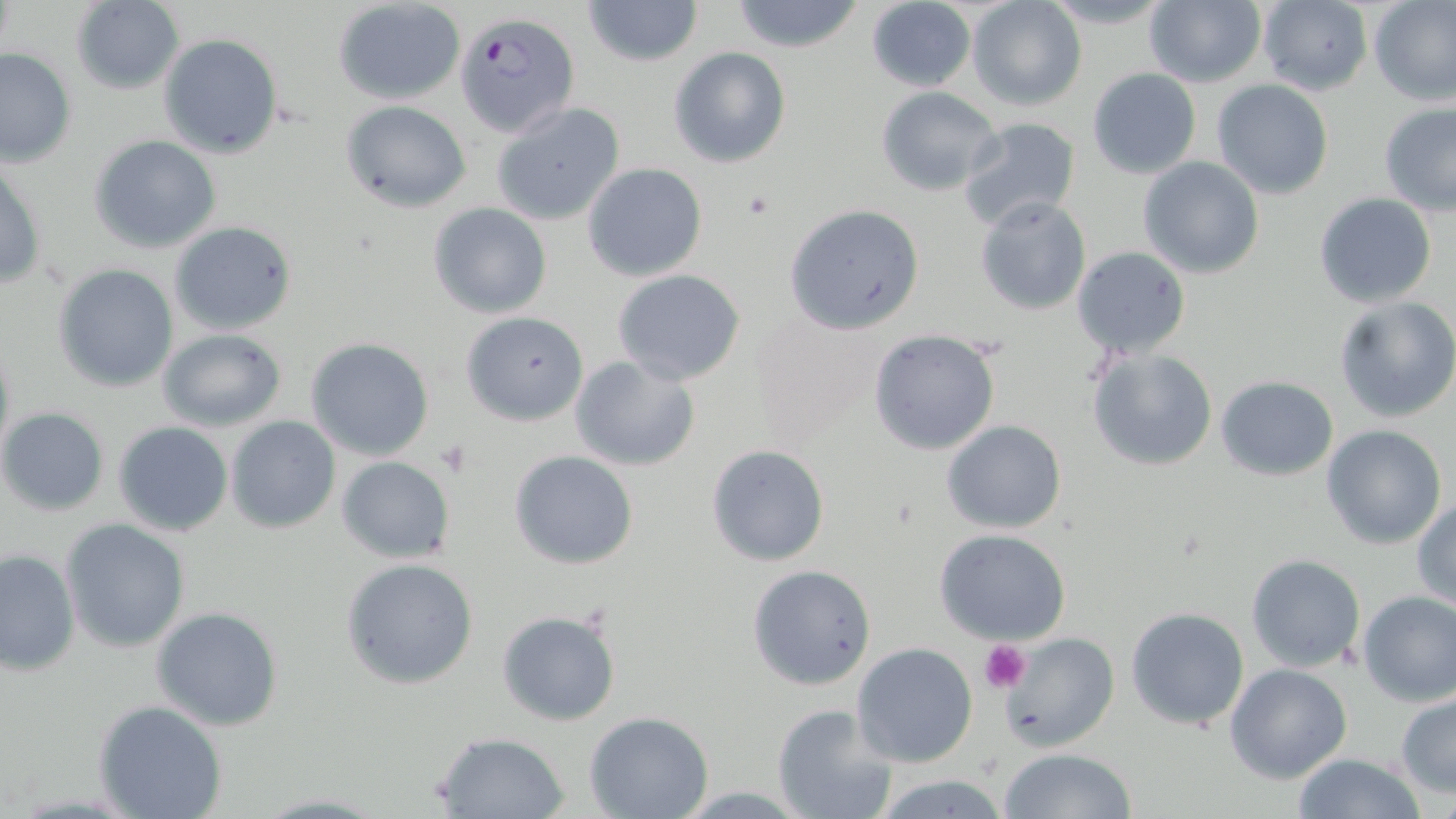
{
  "slide_level_diagnosis": "Plasmodium falciparum",
  "stain": "May-Grünwald-Giemsa",
  "modality": "optical microscopy",
  "magnification": "1000x",
  "uninfected_red_blood_cell_locations": "approximate bounding boxes as (x1,y1)-(x2,y2) corner pairs in pixels: (582,0)-(703,68), (730,0)-(863,52), (866,0)-(976,92), (966,0)-(1086,112), (1040,0)-(1177,31), (1145,0)-(1267,88), (1256,0)-(1374,96), (1369,0)-(1456,107), (69,1)-(184,93), (333,1)-(467,105), (158,33)-(283,159), (668,46)-(791,169), (0,47)-(76,169), (1087,67)-(1202,177), (1211,79)-(1334,200), (877,86)-(1003,195), (340,99)-(472,212), (490,101)-(626,226), (1379,103)-(1456,215), (957,117)-(1083,232), (88,134)-(222,253), (1137,157)-(1265,279), (0,162)-(48,293), (582,162)-(708,281), (1315,193)-(1438,308), (975,195)-(1091,315), (786,202)-(926,335), (428,203)-(552,319), (169,221)-(297,334), (1071,246)-(1191,359), (52,263)-(179,392), (611,269)-(747,386), (1334,296)-(1456,423), (747,309)-(892,445), (460,310)-(589,426), (157,327)-(288,433), (867,328)-(1001,457), (0,333)-(16,468), (306,337)-(434,460), (1085,345)-(1220,471), (569,354)-(700,471), (1214,375)-(1339,481), (1,407)-(109,515), (226,415)-(340,534), (941,420)-(1066,534), (114,421)-(233,536), (1320,424)-(1448,550), (706,444)-(830,567), (509,450)-(638,569), (337,455)-(455,564), (1412,499)-(1456,610), (61,519)-(191,652), (936,529)-(1072,644), (0,547)-(80,675), (1245,554)-(1367,673), (340,557)-(481,689), (746,564)-(877,689), (1356,589)-(1456,706), (151,606)-(284,732), (1125,607)-(1250,730), (497,609)-(621,725), (998,631)-(1119,753), (852,642)-(978,768), (1225,664)-(1353,783), (1396,693)-(1456,797), (95,700)-(226,819), (771,703)-(897,819), (583,712)-(714,819), (430,731)-(570,817), (999,747)-(1136,819), (1290,754)-(1429,818), (866,772)-(1014,819), (249,792)-(389,817)",
  "preparation": "thin blood film",
  "plasmodium_falciparum_infected_red_blood_cell_locations": "approximate bounding boxes as (x1,y1)-(x2,y2) corner pairs in pixels: (455,12)-(579,136)",
  "field_of_view": "single",
  "platelet_locations": "approximate bounding boxes as (x1,y1)-(x2,y2) corner pairs in pixels: (433,440)-(480,479), (980,639)-(1032,693)",
  "image_size": "1456×819 pixels"
}